Outline each Plasmodium vivax-infected red blood cell.
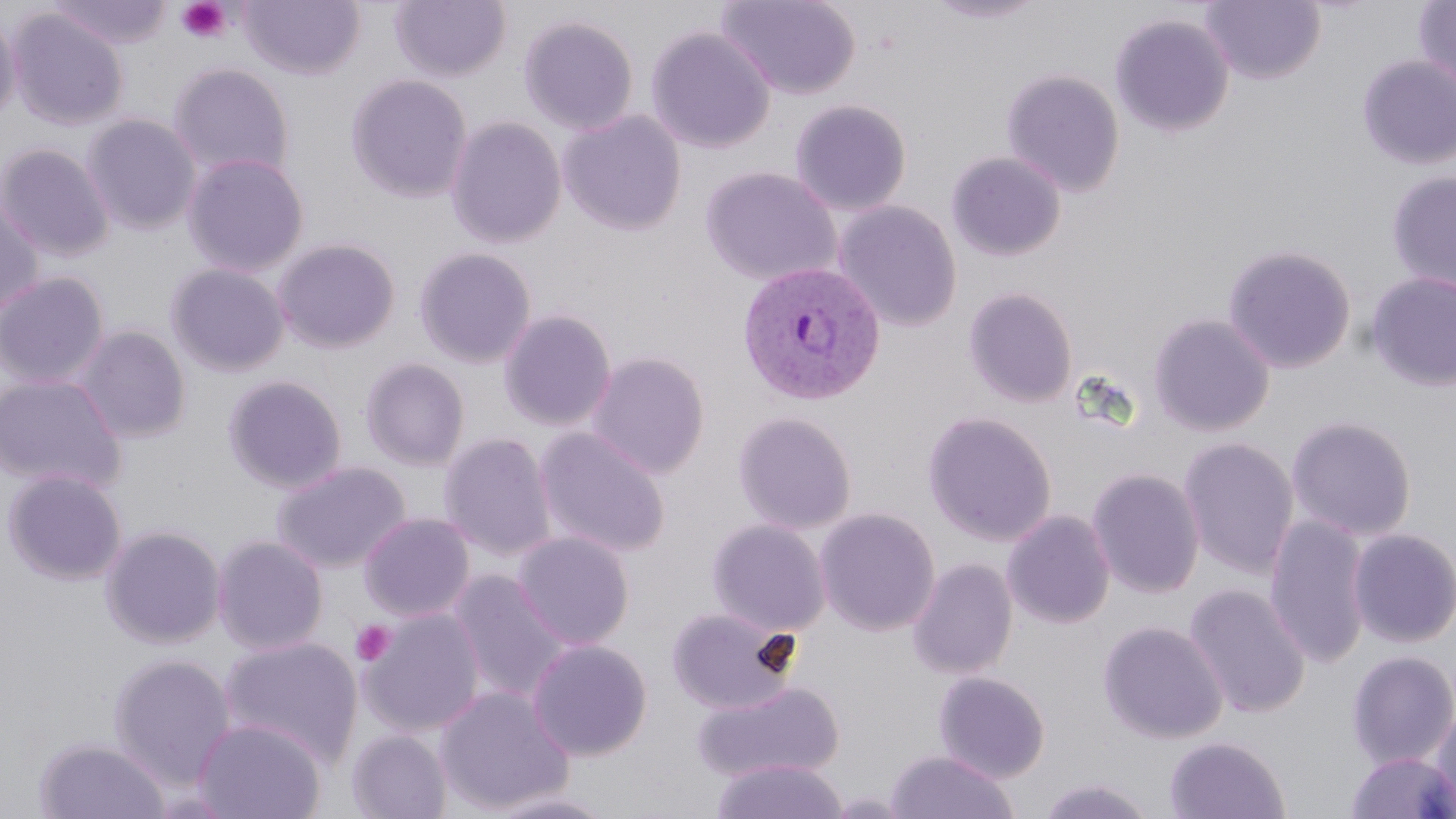
Approximate bounding boxes as (x1, y1, x2, y2) in pixels.
Plasmodium vivax-infected red blood cells: (736, 260, 887, 407).

Uninfected red blood cell locations: (239, 0, 365, 79), (390, 0, 511, 81), (717, 0, 861, 99), (922, 0, 1050, 24), (1201, 0, 1326, 85), (1413, 0, 1456, 96), (46, 1, 173, 50), (0, 9, 21, 125), (7, 9, 128, 131), (1110, 14, 1234, 137), (518, 15, 639, 135), (646, 26, 775, 153), (1357, 55, 1456, 170), (168, 61, 295, 182), (1001, 69, 1125, 197), (346, 74, 473, 203), (790, 99, 912, 216), (558, 110, 686, 236), (80, 113, 202, 235), (445, 115, 566, 249), (0, 143, 115, 262), (947, 151, 1066, 261), (182, 152, 310, 277), (699, 166, 842, 286), (1386, 171, 1456, 295), (0, 195, 44, 318), (834, 201, 962, 331), (273, 238, 401, 354), (1222, 243, 1357, 374), (414, 247, 537, 368), (165, 262, 290, 377), (0, 271, 110, 389), (1366, 271, 1456, 391), (963, 287, 1079, 408), (498, 309, 616, 431), (1148, 313, 1275, 437), (75, 325, 191, 443), (587, 351, 710, 480), (360, 357, 470, 471), (0, 373, 127, 493), (223, 374, 347, 494), (733, 411, 857, 534), (922, 411, 1057, 546), (1286, 415, 1417, 541), (534, 427, 671, 559), (438, 432, 556, 561), (1178, 437, 1300, 579), (272, 461, 411, 574), (2, 468, 128, 585), (1087, 468, 1205, 598), (814, 507, 940, 636), (1002, 510, 1115, 628), (359, 512, 475, 621), (1264, 514, 1372, 669), (707, 519, 831, 637), (100, 524, 226, 649), (1348, 528, 1456, 648), (513, 531, 634, 650), (212, 534, 328, 656), (907, 558, 1018, 680), (449, 570, 570, 703), (1184, 583, 1311, 719), (666, 606, 799, 714), (359, 608, 485, 737), (1098, 620, 1228, 744), (218, 636, 363, 771), (527, 639, 652, 760), (1346, 650, 1456, 769), (108, 653, 236, 791), (933, 671, 1051, 783), (690, 680, 844, 784), (435, 684, 573, 815), (1430, 703, 1456, 818), (192, 716, 326, 819), (348, 728, 452, 819), (1164, 736, 1290, 818), (34, 737, 170, 818), (884, 750, 1019, 819), (1345, 751, 1456, 818), (710, 758, 849, 819), (1036, 776, 1157, 819), (480, 790, 621, 818). Platelet locations: (175, 0, 234, 44), (350, 620, 397, 667). Slide-level diagnosis: Plasmodium vivax. Image is 1456×819 pixels. May-Grünwald-Giemsa stain. Thin blood film. One field of a larger specimen. Optical microscopy. Captured at 1000x magnification.